Identify the cell.
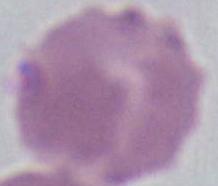

This is an erythrocyte.

magnification = 1000x
modality = photomicrograph